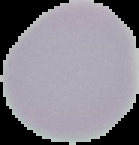

Summary:
  - Image size: 139×145 pixels
  - Preparation: thin blood smear
  - Result: no malaria parasites detected
  - Image type: segmented cell region on a black background